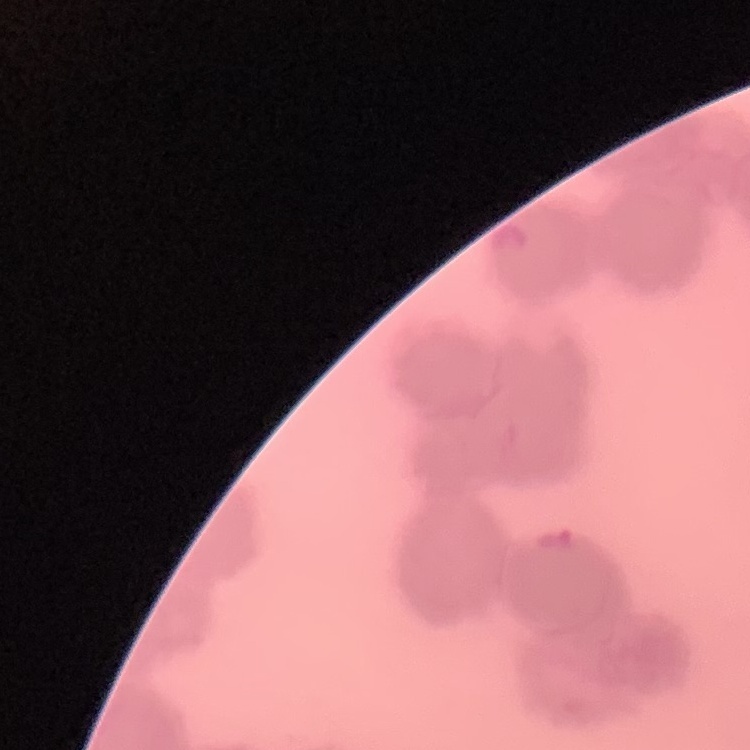
{
  "red_blood_cell_morphology": "rouleaux formation",
  "preparation": "thin blood smear",
  "stain": "Field's or Giemsa",
  "image_type": "one tile cut from a larger photomicrograph"
}